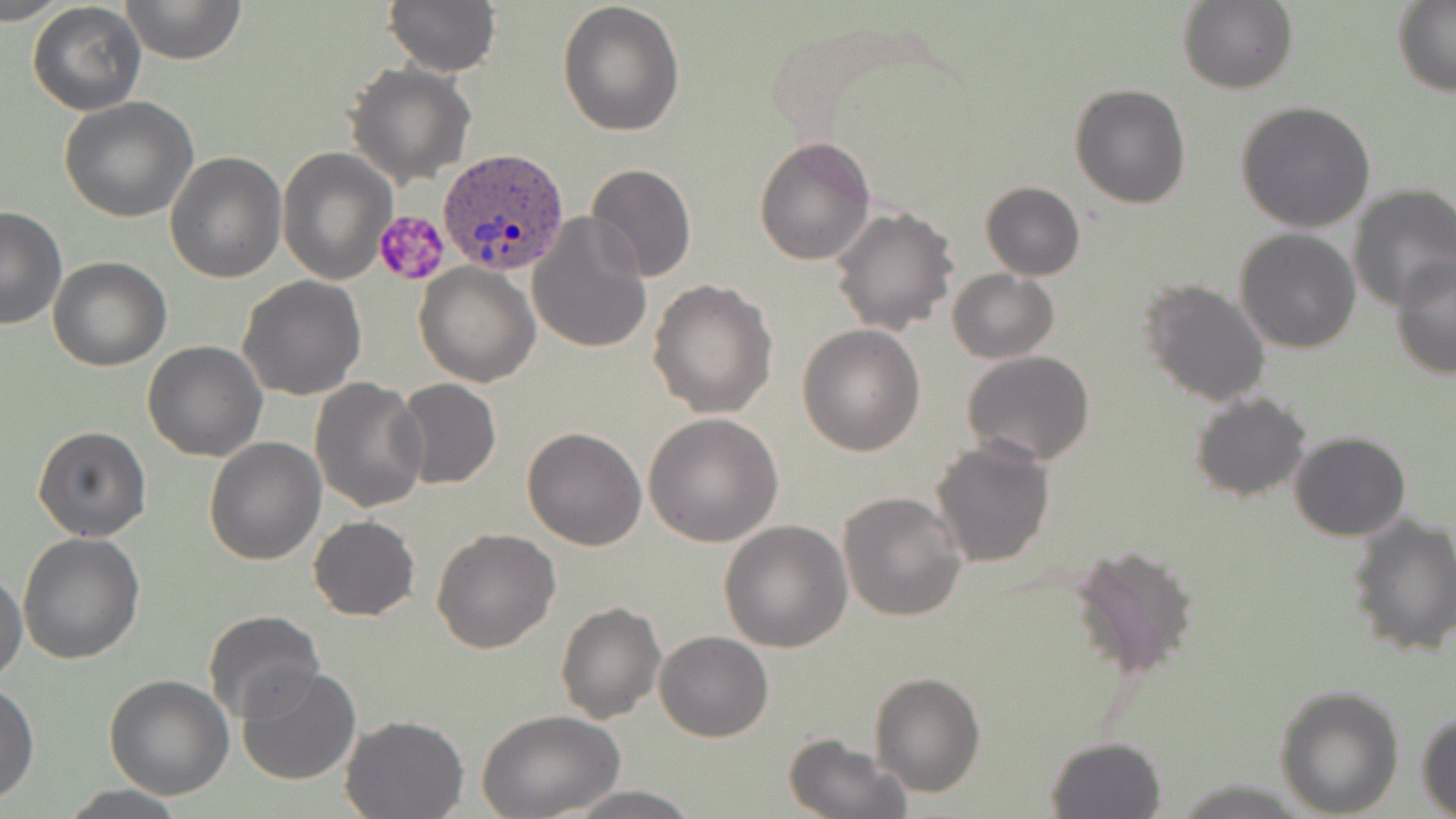

Approximate bounding boxes as [x1, y1, x2, y2] in pixels. Platelet locations: [373, 209, 451, 286]. Uninfected red blood cell locations: [1, 0, 64, 27], [120, 0, 246, 64], [383, 0, 502, 77], [558, 1, 687, 137], [1177, 1, 1297, 95], [27, 2, 146, 116], [1392, 2, 1456, 95], [345, 62, 475, 187], [1070, 83, 1191, 209], [59, 96, 199, 223], [1234, 100, 1376, 233], [754, 135, 875, 266], [277, 147, 395, 283], [165, 152, 286, 283], [585, 163, 697, 283], [980, 182, 1085, 280], [1347, 184, 1456, 309], [832, 205, 958, 336], [1, 207, 66, 331], [528, 213, 653, 355], [1234, 226, 1362, 354], [1389, 255, 1455, 381], [47, 257, 172, 371], [415, 261, 541, 387], [947, 269, 1059, 364], [236, 275, 367, 400], [1139, 278, 1273, 408], [649, 279, 779, 418], [796, 324, 925, 456], [143, 340, 268, 460], [961, 349, 1097, 465], [310, 377, 430, 512], [393, 378, 502, 489], [1189, 391, 1312, 501], [643, 413, 783, 547], [32, 425, 150, 542], [521, 425, 648, 549], [1288, 430, 1412, 542], [203, 436, 327, 566], [929, 438, 1056, 570], [838, 490, 967, 623], [1345, 512, 1456, 660], [308, 515, 420, 621], [718, 519, 853, 651], [431, 527, 560, 652], [18, 533, 146, 665], [1069, 540, 1201, 680], [1, 568, 27, 685], [555, 599, 667, 724], [203, 610, 324, 722], [654, 630, 774, 742], [235, 664, 363, 788], [102, 673, 234, 799], [870, 673, 985, 797], [0, 680, 38, 805], [1273, 682, 1405, 816], [479, 709, 626, 817], [1416, 710, 1456, 818], [341, 715, 470, 819], [781, 733, 911, 819], [1044, 735, 1167, 818], [58, 785, 192, 818], [557, 785, 703, 818]. Plasmodium ovale-infected red blood cell locations: [437, 146, 570, 275]. Slide-level diagnosis: Plasmodium ovale. 1000x magnification. May-Grünwald-Giemsa stain. One field of a larger specimen. Optical microscopy. Thin blood film. Image is 1456×819 pixels.